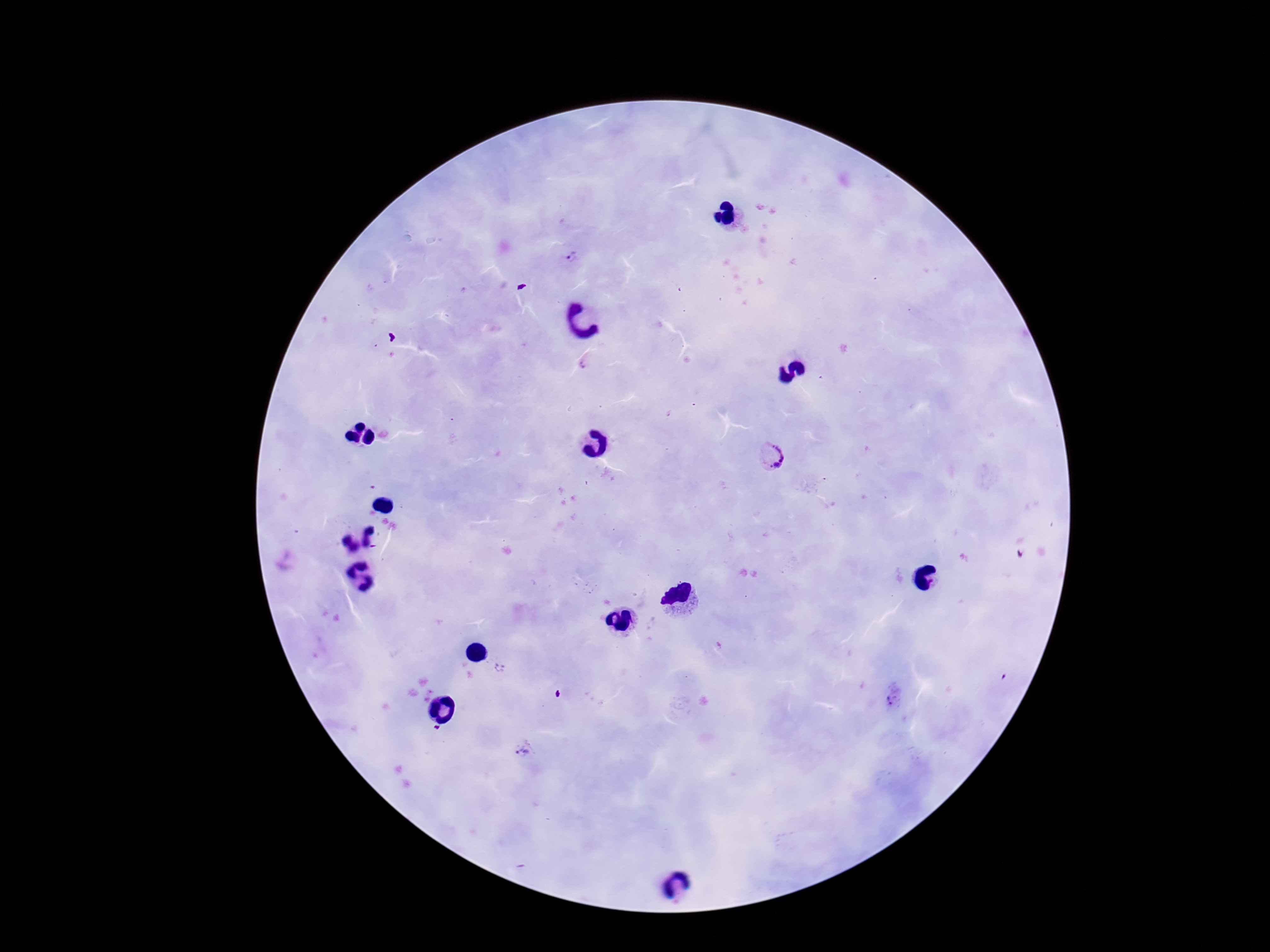

Approximate centers as [x, y] in pixels.
Summary:
  - Plasmodium parasite locations: [572, 257], [584, 364], [773, 457], [892, 700], [523, 751]
  - Preparation: thick blood film
  - Patient malaria status: infected
  - Field of view: single
  - Capture: smartphone camera through the microscope eyepiece
  - Stain: Giemsa
  - Image size: 1270×952 pixels
  - Magnification: 100x